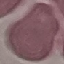

Summary:
  - Malaria status: uninfected
  - Capture: smartphone through the microscope eyepiece
  - Preparation: thin smear
  - Stain: Giemsa
  - Image type: automatically extracted cell patch, resized to 64 × 64 pixels